Assess the morphology of the red blood cells.
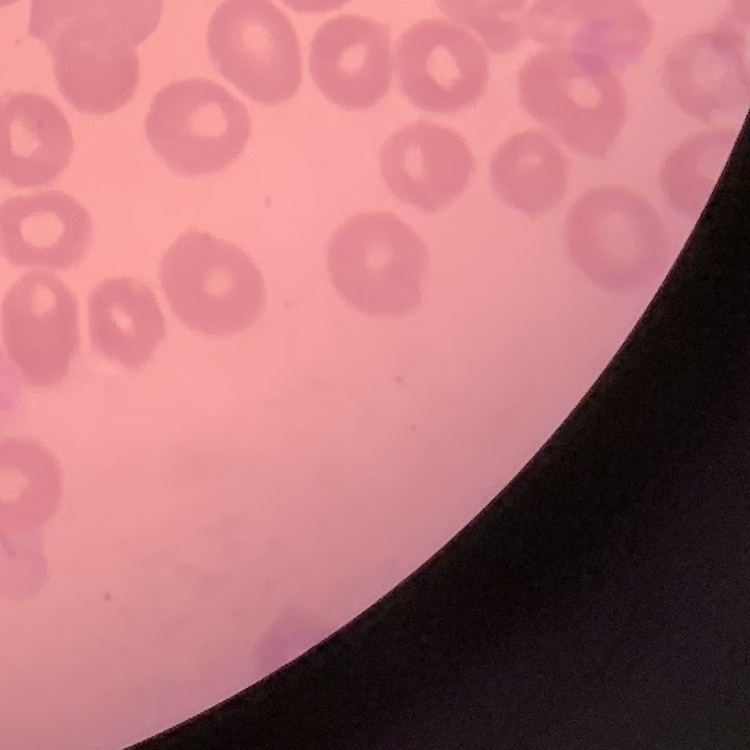
No rouleaux formation.

stain = Field's or Giemsa
image type = square crop of a larger photomicrograph
preparation = thin peripheral smear